Locate every blood parasite and identify its species.
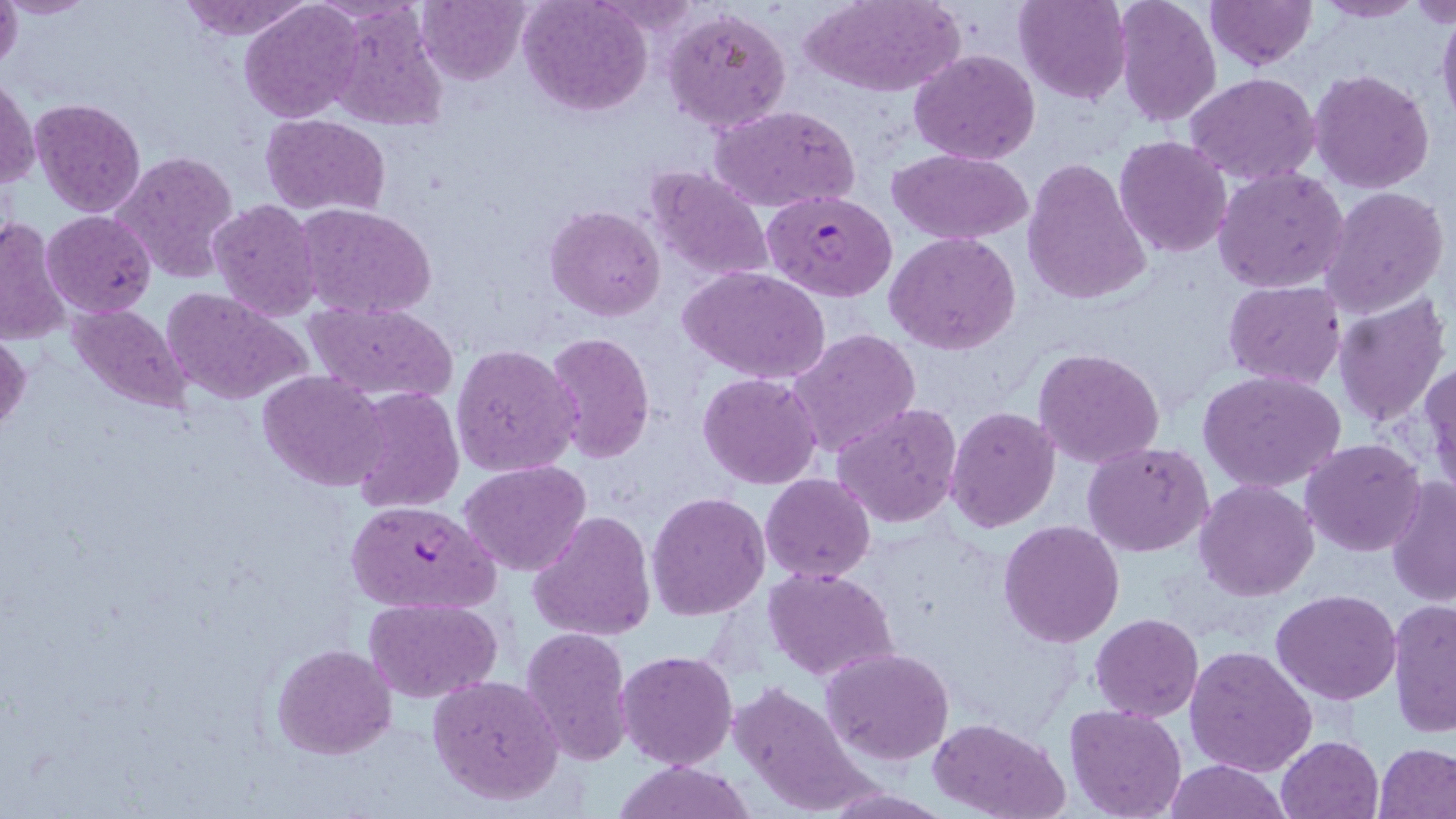

Approximate bounding boxes as (x1,y1)-(x2,y2) corner pairs in pixels.
Plasmodium falciparum-infected red blood cells: (761,190)-(897,303), (343,499)-(501,615).
No Plasmodium ovale, Plasmodium malariae, Plasmodium vivax, Babesia divergens, or Trypanosoma brucei observed.

Uninfected red blood cell locations: (0,0)-(22,72), (1,0)-(98,19), (175,0)-(311,41), (416,0)-(530,85), (518,0)-(652,115), (802,0)-(964,97), (1013,0)-(1130,104), (1114,0)-(1222,126), (1205,0)-(1317,71), (1312,0)-(1423,23), (1406,0)-(1456,27), (240,1)-(364,122), (1436,4)-(1456,132), (663,5)-(792,134), (323,6)-(449,131), (909,48)-(1041,165), (1309,68)-(1436,193), (1185,72)-(1321,186), (1,74)-(38,191), (1148,82)-(1283,218), (30,98)-(145,216), (709,104)-(860,212), (260,114)-(391,216), (1114,135)-(1233,257), (889,149)-(1034,245), (111,150)-(240,283), (1021,159)-(1152,305), (643,166)-(774,284), (1213,166)-(1351,295), (1320,186)-(1449,321), (207,199)-(323,320), (293,203)-(437,319), (545,205)-(666,321), (41,210)-(156,318), (0,215)-(72,345), (884,232)-(1021,355), (681,266)-(831,384), (1222,280)-(1345,388), (159,287)-(307,407), (1332,294)-(1449,428), (69,302)-(194,415), (305,302)-(460,403), (787,327)-(921,458), (0,328)-(31,435), (542,332)-(654,465), (450,343)-(580,478), (1034,347)-(1166,466), (1423,359)-(1456,494), (259,371)-(387,493), (1198,371)-(1347,493), (697,372)-(824,491), (348,387)-(464,515), (831,402)-(964,530), (945,406)-(1061,534), (1300,438)-(1425,557), (1084,443)-(1214,558), (459,460)-(592,576), (759,474)-(876,584), (1387,478)-(1456,605), (1194,480)-(1320,602), (647,492)-(770,620), (529,511)-(655,644), (998,519)-(1125,647), (764,565)-(898,681), (1271,588)-(1402,705), (364,596)-(501,704), (1387,599)-(1454,738), (1090,613)-(1204,720), (521,626)-(634,764), (271,643)-(398,760), (1184,644)-(1317,777), (823,646)-(954,766), (616,649)-(739,771), (428,674)-(565,805), (728,679)-(871,814), (1064,704)-(1187,819), (930,717)-(1067,819), (1275,734)-(1384,819), (1374,743)-(1456,818), (1161,759)-(1292,818), (610,760)-(758,818). Slide-level diagnosis: Plasmodium falciparum. Thin blood smear. One field of a larger specimen. Image is 1456×819 pixels. May-Grünwald-Giemsa-stained preparation. Captured at 1000x magnification. Optical microscopy.